Assess the morphology of the erythrocytes.
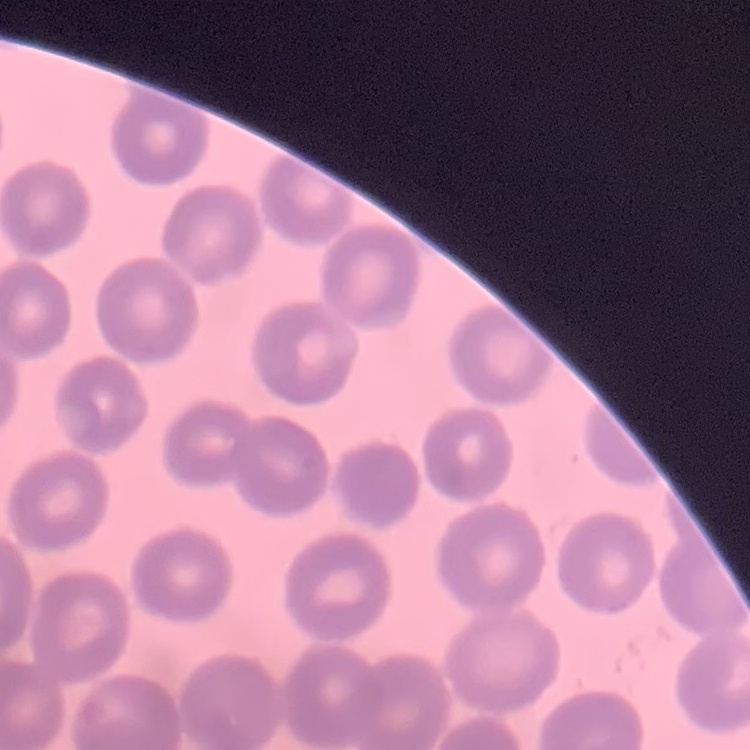

No rouleaux formation.

Square crop of a larger photomicrograph. Stained with either Field's or Giemsa. Thin blood smear.